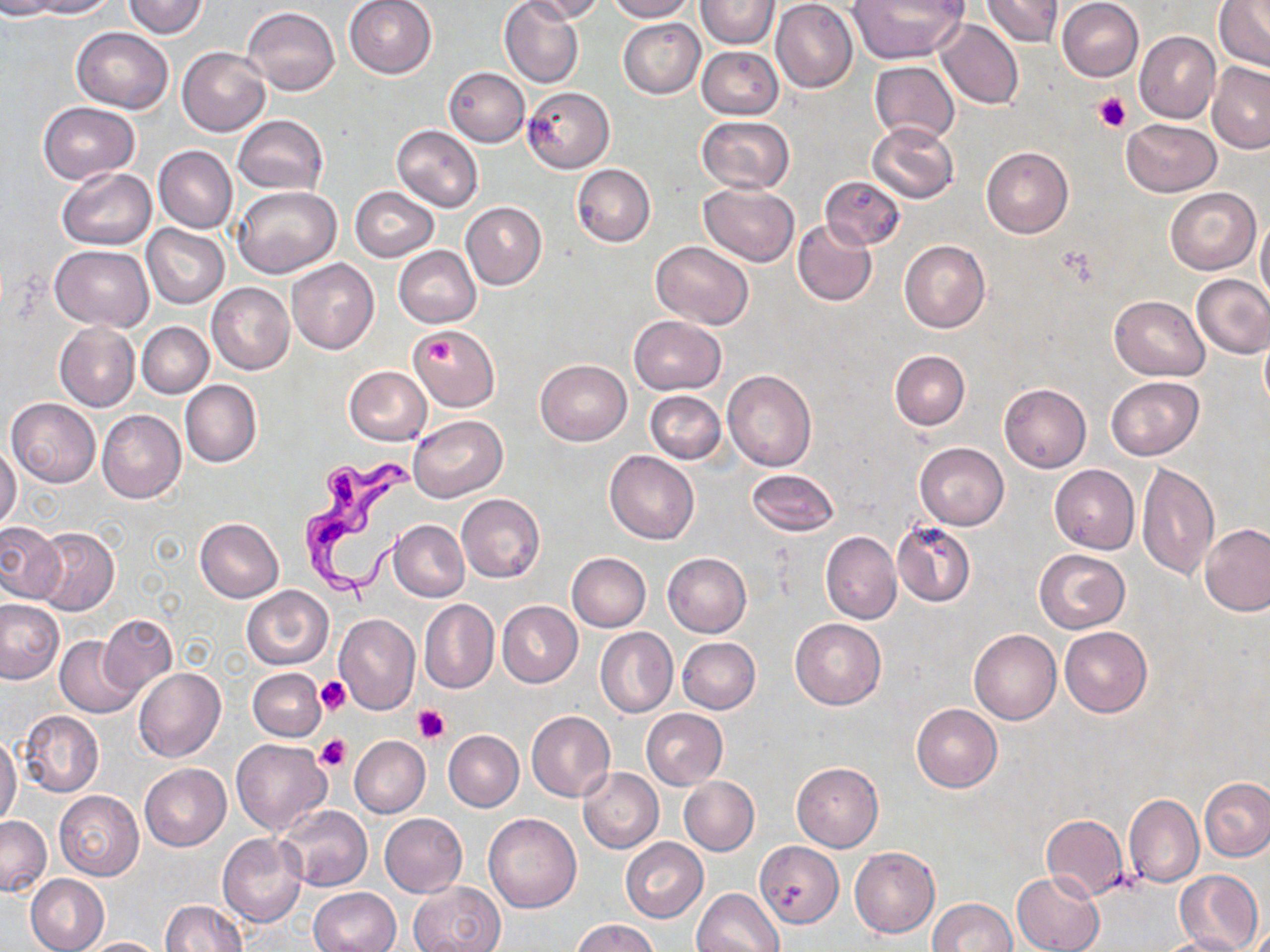
Summary:
  - Coordinate format: approximate bounding boxes as (x1, y1, x2, y2) in pixels
  - Platelet locations: (1095, 92, 1131, 134), (415, 332, 459, 370), (317, 677, 351, 714), (413, 705, 450, 744), (317, 734, 351, 772)
  - Uninfected red blood cell locations: (0, 0, 60, 19), (26, 0, 116, 18), (122, 0, 209, 38), (343, 0, 438, 79), (500, 0, 583, 88), (521, 0, 605, 22), (606, 0, 695, 22), (697, 0, 780, 49), (771, 0, 858, 93), (848, 0, 966, 64), (980, 0, 1064, 50), (1056, 0, 1144, 81), (1213, 1, 1270, 72), (773, 4, 957, 81), (243, 7, 340, 95), (619, 19, 704, 98), (935, 19, 1023, 110), (71, 27, 173, 112), (1135, 31, 1221, 122), (179, 47, 271, 135), (697, 47, 783, 120), (870, 61, 960, 145), (1207, 62, 1270, 152), (444, 67, 530, 146), (521, 86, 614, 173), (39, 102, 139, 183), (696, 115, 794, 193), (233, 116, 328, 194), (1121, 118, 1221, 197), (866, 122, 960, 204), (391, 125, 483, 211), (154, 145, 237, 233), (981, 147, 1073, 238), (572, 164, 655, 247), (56, 168, 156, 250), (819, 174, 904, 249), (698, 182, 800, 265), (233, 186, 340, 279), (350, 186, 437, 261), (1165, 186, 1260, 275), (461, 202, 547, 289), (1256, 215, 1270, 306), (792, 219, 877, 307), (141, 224, 229, 308), (899, 240, 990, 333), (651, 241, 753, 329), (51, 246, 154, 330), (393, 247, 481, 329), (287, 259, 379, 354), (1192, 274, 1270, 358), (206, 282, 294, 375), (1109, 295, 1210, 380), (628, 315, 726, 394), (54, 322, 140, 411), (138, 322, 213, 398), (409, 324, 499, 411), (890, 350, 970, 430), (535, 359, 631, 445), (343, 366, 431, 445), (722, 369, 817, 471), (1105, 375, 1203, 461), (180, 380, 261, 468), (999, 384, 1091, 472), (646, 390, 726, 464), (7, 398, 99, 487), (97, 409, 186, 503), (409, 415, 507, 502), (914, 441, 1009, 530), (0, 446, 21, 530), (605, 450, 700, 544), (1137, 462, 1219, 580), (1050, 464, 1139, 553), (745, 469, 839, 537), (456, 494, 545, 582), (195, 518, 284, 603), (390, 519, 469, 602), (0, 521, 65, 603), (891, 521, 975, 608), (1201, 524, 1270, 616), (33, 527, 120, 615), (821, 530, 901, 624), (1035, 549, 1130, 633), (662, 552, 752, 637), (566, 553, 650, 631), (242, 585, 334, 670), (0, 598, 66, 684), (419, 599, 498, 694), (496, 601, 583, 688), (333, 613, 420, 715), (100, 614, 177, 695), (790, 618, 885, 708), (1060, 626, 1153, 717), (595, 627, 678, 718), (969, 630, 1061, 724), (55, 635, 144, 717), (678, 638, 760, 714), (133, 667, 225, 763), (249, 667, 326, 741), (911, 703, 1001, 792), (641, 708, 727, 789), (18, 709, 103, 797), (526, 711, 616, 802), (443, 730, 524, 811), (0, 735, 21, 827), (349, 735, 430, 817), (230, 739, 331, 836), (792, 762, 884, 852), (140, 763, 232, 851), (579, 767, 663, 852), (678, 776, 759, 856), (1199, 777, 1270, 861), (54, 791, 143, 880), (1124, 794, 1203, 888), (277, 804, 372, 891), (1044, 805, 1199, 890), (483, 812, 582, 912), (380, 813, 467, 897), (1040, 814, 1128, 901), (0, 815, 51, 896), (218, 833, 307, 927), (620, 838, 708, 922), (756, 840, 842, 926), (850, 847, 940, 938), (1173, 869, 1263, 952), (1012, 871, 1104, 952), (26, 874, 108, 952), (407, 881, 504, 952), (308, 887, 401, 952), (693, 888, 784, 952), (926, 898, 1019, 952), (160, 900, 246, 952), (571, 919, 658, 952), (1151, 934, 1249, 952), (80, 937, 166, 951)
  - Trypanosoma brucei locations: (296, 455, 421, 594)
  - Slide-level diagnosis: Trypanosoma brucei
  - Magnification: 1000x
  - Stain: May-Grünwald-Giemsa
  - Image size: 1270×952 pixels
  - Preparation: thin blood film
  - Field of view: one of a larger specimen
  - Modality: light microscopy